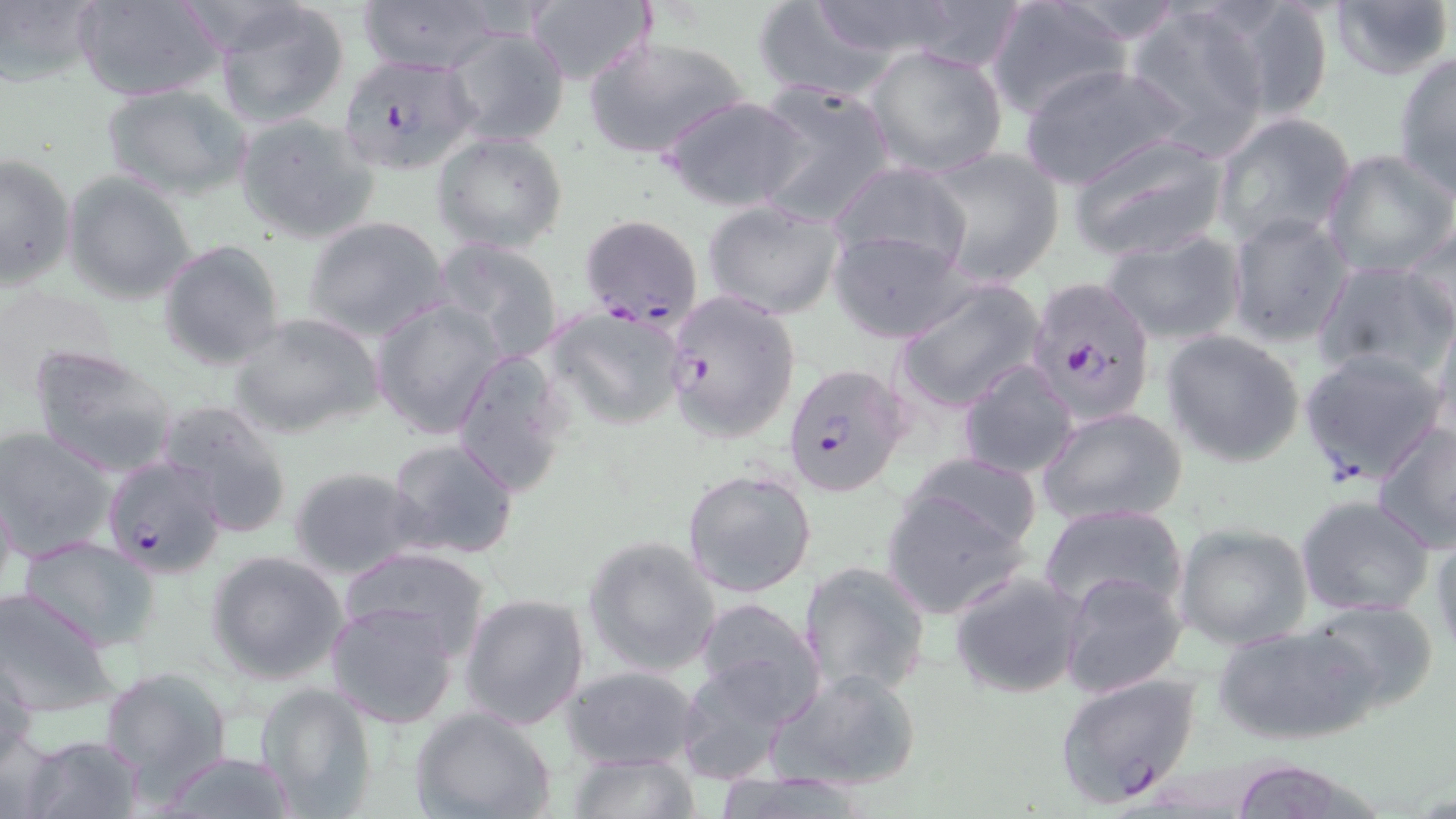

Summary:
  - Coordinate format: approximate bounding boxes as (x1, y1, x2, y2) in pixels
  - Plasmodium falciparum-infected red blood cell locations: (336, 53, 479, 174), (580, 213, 704, 331), (1028, 279, 1148, 432), (664, 289, 800, 444), (1298, 349, 1449, 487), (781, 361, 911, 499), (102, 455, 229, 580), (1053, 671, 1202, 807)
  - Uninfected red blood cell locations: (0, 0, 103, 89), (72, 0, 230, 103), (359, 0, 502, 74), (751, 0, 904, 103), (803, 0, 966, 62), (983, 0, 1131, 122), (1210, 0, 1336, 122), (1325, 0, 1453, 82), (525, 1, 655, 87), (211, 3, 352, 128), (1122, 5, 1273, 155), (444, 28, 571, 148), (584, 35, 748, 159), (864, 41, 1010, 178), (1393, 52, 1456, 198), (1016, 63, 1194, 191), (99, 82, 250, 201), (749, 82, 896, 228), (660, 94, 809, 212), (1211, 111, 1357, 248), (234, 113, 379, 244), (433, 131, 569, 253), (1067, 132, 1231, 262), (919, 146, 1067, 288), (1321, 149, 1455, 278), (0, 150, 77, 291), (827, 160, 975, 277), (64, 170, 199, 305), (702, 199, 845, 320), (1226, 212, 1354, 348), (302, 216, 450, 340), (1401, 220, 1455, 340), (1101, 228, 1247, 347), (829, 230, 970, 342), (431, 238, 567, 363), (158, 240, 287, 370), (1313, 259, 1454, 383), (896, 277, 1048, 415), (0, 282, 125, 390), (370, 298, 506, 439), (546, 306, 690, 428), (1429, 307, 1456, 440), (229, 312, 385, 440), (1161, 328, 1306, 467), (28, 344, 180, 478), (448, 346, 574, 497), (956, 360, 1080, 480), (157, 398, 293, 537), (1036, 406, 1187, 527), (1372, 420, 1455, 555), (0, 427, 119, 560), (385, 436, 520, 562), (907, 453, 1043, 552), (287, 465, 426, 579), (682, 466, 817, 600), (0, 475, 17, 610), (881, 485, 1030, 619), (1295, 494, 1434, 617), (1037, 503, 1189, 620), (1174, 521, 1314, 650), (1431, 531, 1456, 659), (14, 534, 160, 652), (582, 535, 722, 678), (338, 545, 492, 662), (205, 549, 350, 684), (797, 559, 932, 700), (947, 570, 1088, 700), (1057, 570, 1187, 701), (0, 587, 119, 715), (459, 592, 590, 730), (692, 595, 826, 719), (1304, 596, 1440, 711), (323, 600, 461, 729), (1214, 624, 1376, 745), (1, 650, 39, 765), (673, 657, 799, 787), (563, 665, 702, 771), (98, 666, 231, 791), (769, 666, 924, 792), (253, 681, 378, 816), (411, 706, 556, 819), (0, 724, 58, 819), (16, 732, 145, 819), (153, 750, 301, 818), (568, 753, 700, 819), (1223, 759, 1370, 819)
  - Slide-level diagnosis: Plasmodium falciparum
  - Field of view: single
  - Stain: May-Grünwald-Giemsa
  - Magnification: 1000x
  - Modality: optical microscopy
  - Image size: 1456×819 pixels
  - Preparation: thin blood film